Outline platelets.
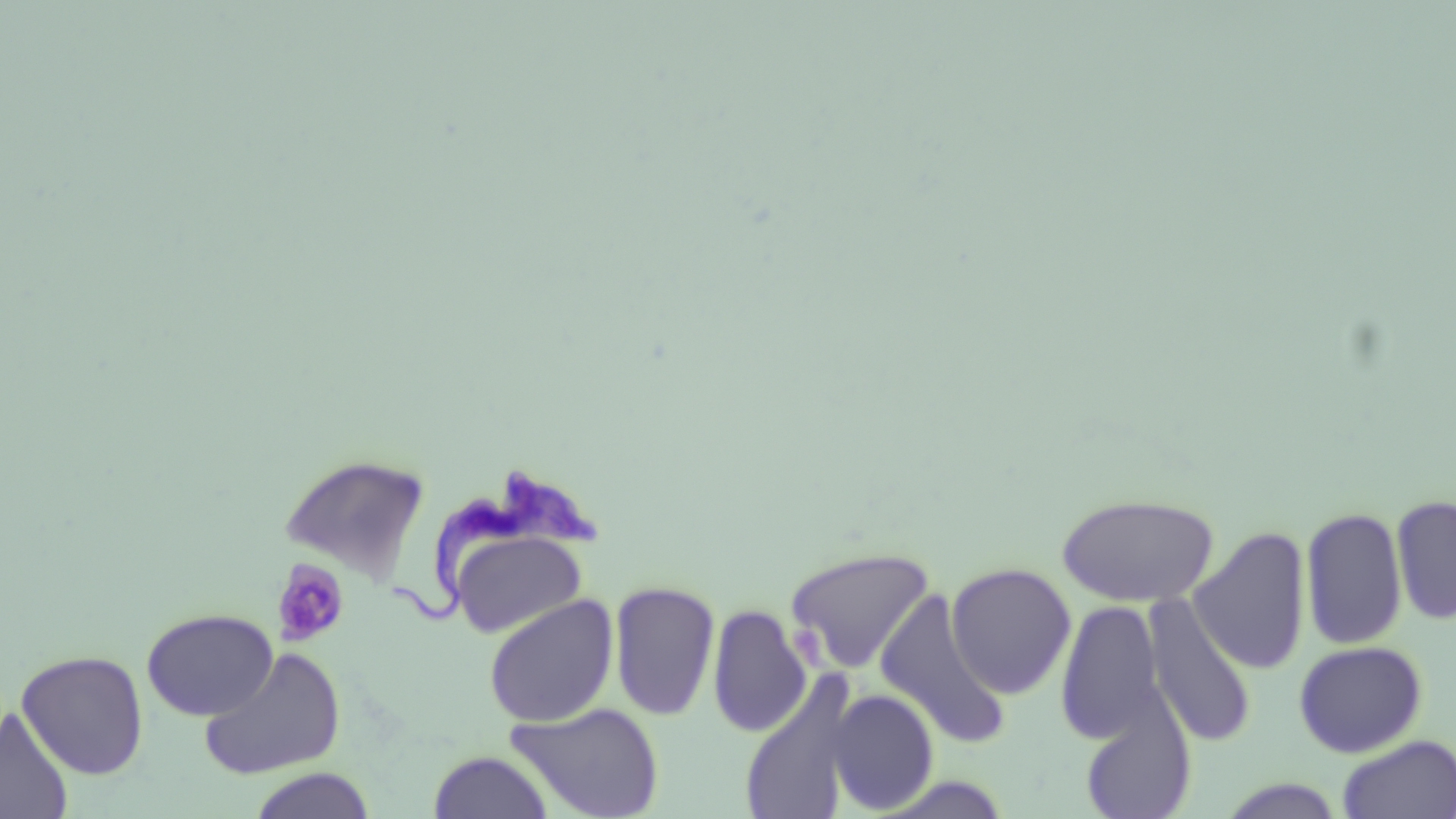

Approximate bounding boxes as [x1, y1, x2, y2] in pixels.
Platelets: [270, 557, 351, 649], [790, 623, 826, 664].

Summary:
  - Uninfected red blood cell locations: [278, 453, 431, 582], [1056, 492, 1220, 607], [1391, 493, 1456, 626], [1300, 505, 1408, 650], [1191, 525, 1312, 675], [449, 529, 587, 638], [783, 546, 937, 674], [946, 562, 1077, 699], [609, 578, 721, 722], [874, 587, 1010, 748], [1143, 594, 1257, 748], [484, 595, 619, 727], [1054, 597, 1167, 747], [709, 604, 811, 739], [142, 607, 278, 720], [1293, 640, 1428, 758], [198, 646, 346, 780], [16, 649, 149, 780], [737, 670, 860, 819], [826, 689, 940, 814], [1078, 700, 1198, 819], [507, 702, 664, 819], [1, 707, 74, 819], [1336, 735, 1456, 819], [428, 750, 554, 819], [247, 769, 378, 819], [1214, 777, 1346, 818]
  - Trypanosoma brucei locations: [388, 467, 599, 620]
  - Slide-level diagnosis: Trypanosoma brucei
  - Modality: light microscopy
  - Magnification: 1000x
  - Preparation: thin blood film
  - Image size: 1456×819 pixels
  - Stain: May-Grünwald-Giemsa
  - Field of view: single